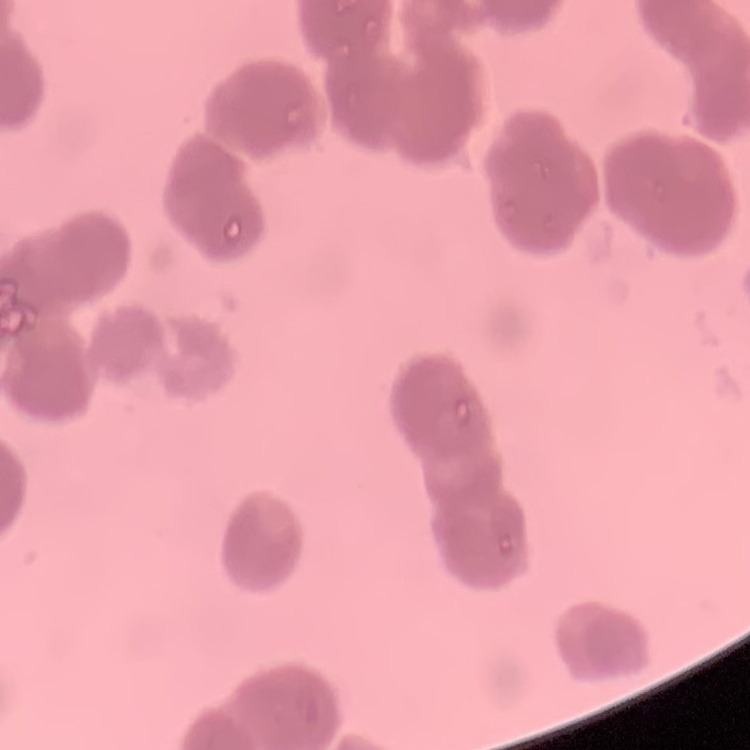

Summary:
  - Red blood cell morphology: rouleaux formation
  - Image type: one tile cut from a larger photomicrograph
  - Stain: Field's or Giemsa
  - Preparation: thin blood film